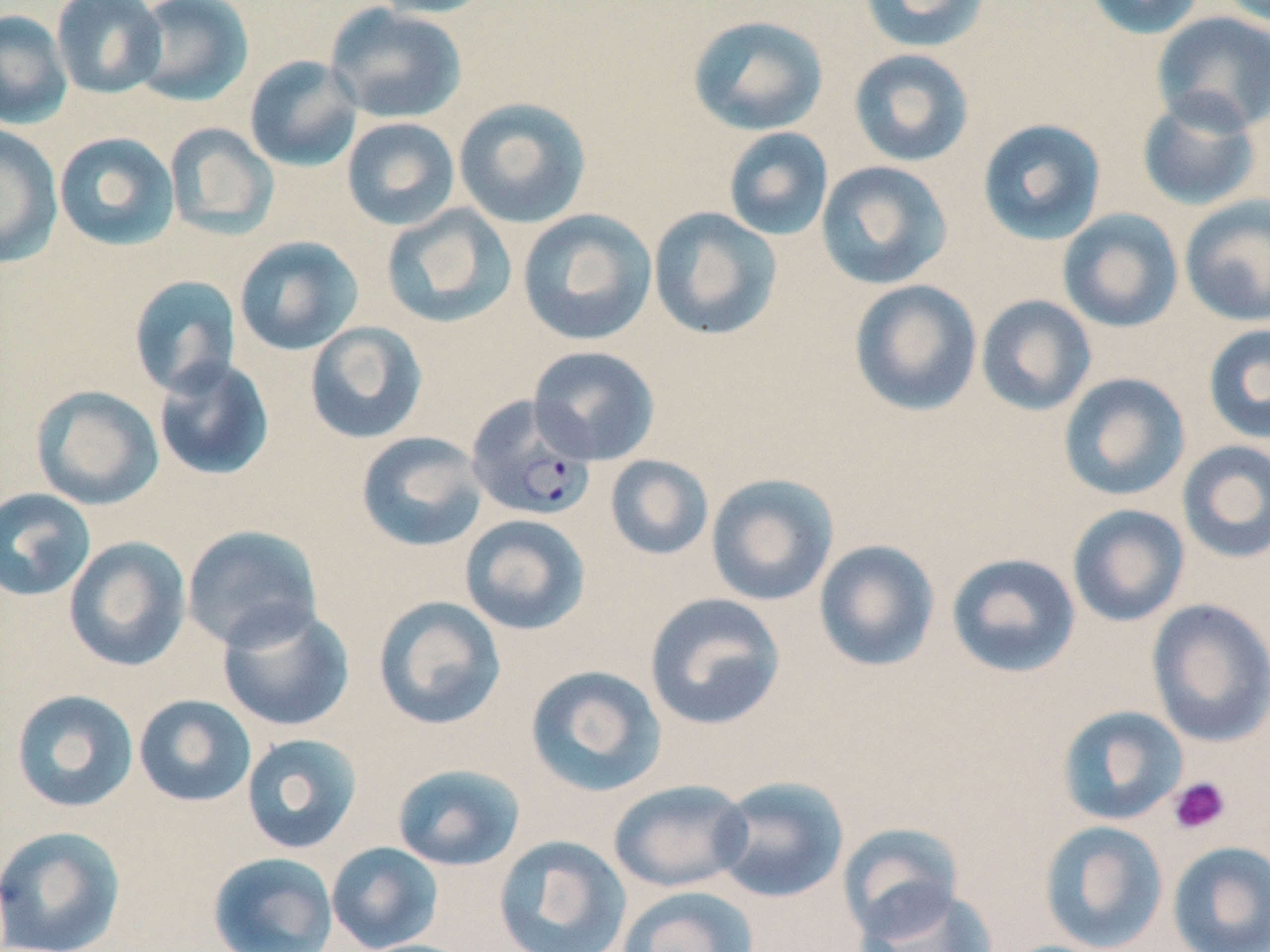 Approximate bounding boxes as named x1/y1/x2/y2 corners in pixels. Uninfected red blood cell locations: (x1=50, y1=0, x2=168, y2=100), (x1=130, y1=0, x2=255, y2=107), (x1=366, y1=0, x2=498, y2=19), (x1=1083, y1=0, x2=1207, y2=40), (x1=858, y1=1, x2=990, y2=52), (x1=1218, y1=1, x2=1270, y2=29), (x1=325, y1=3, x2=467, y2=125), (x1=0, y1=9, x2=72, y2=129), (x1=1151, y1=11, x2=1270, y2=135), (x1=687, y1=14, x2=829, y2=136), (x1=848, y1=49, x2=975, y2=167), (x1=244, y1=55, x2=363, y2=173), (x1=1136, y1=92, x2=1263, y2=212), (x1=453, y1=96, x2=592, y2=229), (x1=341, y1=116, x2=460, y2=231), (x1=976, y1=117, x2=1107, y2=245), (x1=164, y1=122, x2=279, y2=240), (x1=0, y1=125, x2=63, y2=268), (x1=723, y1=127, x2=833, y2=241), (x1=53, y1=131, x2=181, y2=251), (x1=816, y1=160, x2=953, y2=290), (x1=1179, y1=194, x2=1270, y2=327), (x1=381, y1=204, x2=516, y2=329), (x1=648, y1=206, x2=783, y2=342), (x1=517, y1=209, x2=658, y2=346), (x1=1057, y1=209, x2=1184, y2=333), (x1=233, y1=235, x2=363, y2=356), (x1=128, y1=274, x2=242, y2=397), (x1=849, y1=279, x2=982, y2=416), (x1=976, y1=295, x2=1097, y2=416), (x1=303, y1=321, x2=428, y2=445), (x1=1202, y1=323, x2=1270, y2=444), (x1=527, y1=346, x2=660, y2=465), (x1=153, y1=356, x2=275, y2=482), (x1=1057, y1=372, x2=1191, y2=502), (x1=30, y1=384, x2=165, y2=511), (x1=356, y1=431, x2=489, y2=553), (x1=1176, y1=440, x2=1270, y2=564), (x1=604, y1=454, x2=714, y2=561), (x1=705, y1=473, x2=839, y2=607), (x1=0, y1=488, x2=96, y2=602), (x1=1067, y1=504, x2=1190, y2=627), (x1=459, y1=514, x2=591, y2=635), (x1=181, y1=525, x2=322, y2=652), (x1=63, y1=536, x2=192, y2=672), (x1=813, y1=539, x2=940, y2=672), (x1=945, y1=552, x2=1081, y2=678), (x1=644, y1=592, x2=786, y2=731), (x1=372, y1=595, x2=507, y2=731), (x1=1146, y1=598, x2=1270, y2=748), (x1=217, y1=602, x2=355, y2=732), (x1=524, y1=664, x2=668, y2=797), (x1=10, y1=689, x2=139, y2=813), (x1=133, y1=694, x2=257, y2=808), (x1=1056, y1=705, x2=1188, y2=826), (x1=240, y1=733, x2=364, y2=855), (x1=391, y1=763, x2=526, y2=872), (x1=712, y1=776, x2=850, y2=904), (x1=607, y1=779, x2=753, y2=893), (x1=1039, y1=821, x2=1169, y2=951), (x1=837, y1=822, x2=963, y2=940), (x1=0, y1=825, x2=126, y2=952), (x1=493, y1=835, x2=632, y2=952), (x1=326, y1=841, x2=444, y2=952), (x1=1167, y1=841, x2=1270, y2=952), (x1=207, y1=851, x2=339, y2=952), (x1=856, y1=883, x2=999, y2=952), (x1=616, y1=884, x2=760, y2=952). Platelet locations: (x1=1168, y1=776, x2=1231, y2=835). Plasmodium falciparum-infected red blood cell locations: (x1=466, y1=395, x2=597, y2=522). Slide-level diagnosis: Plasmodium falciparum. One field of a larger specimen. Light microscopy. 1000x magnification. May-Grünwald-Giemsa-stained preparation. Thin blood smear. Image is 1270×952 pixels.